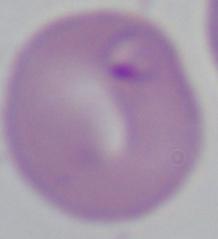

identification: Babesia
magnification: 1000x
modality: micrograph